Comment on the morphology of the red blood cells.
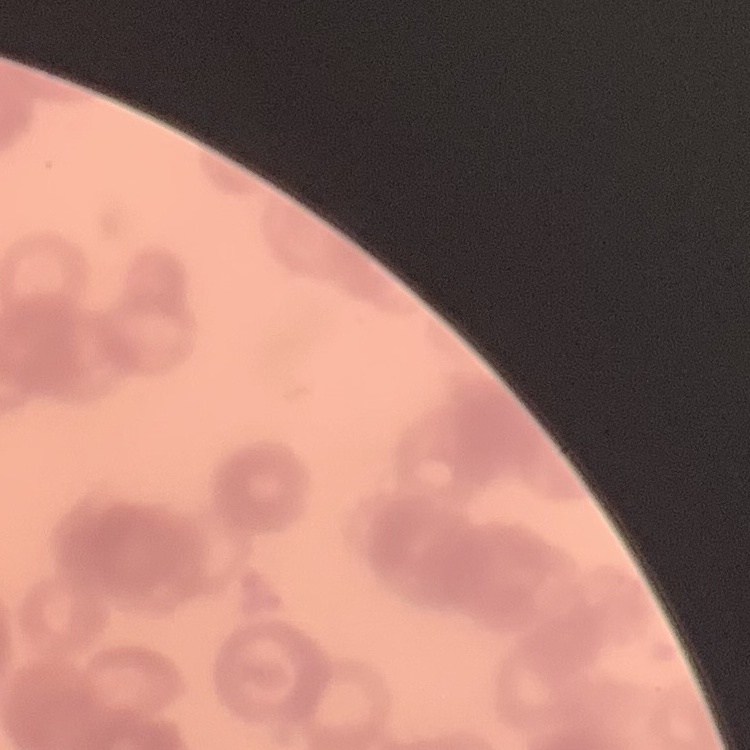

Rouleaux formation.

Thin peripheral smear. One tile cut from a larger photomicrograph. Stained with either Field's or Giemsa.